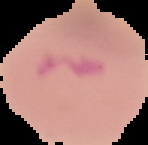

Image is 148×145 pixels. Segmented cell region on a black background. Result: malaria parasites detected. From a thin blood film.